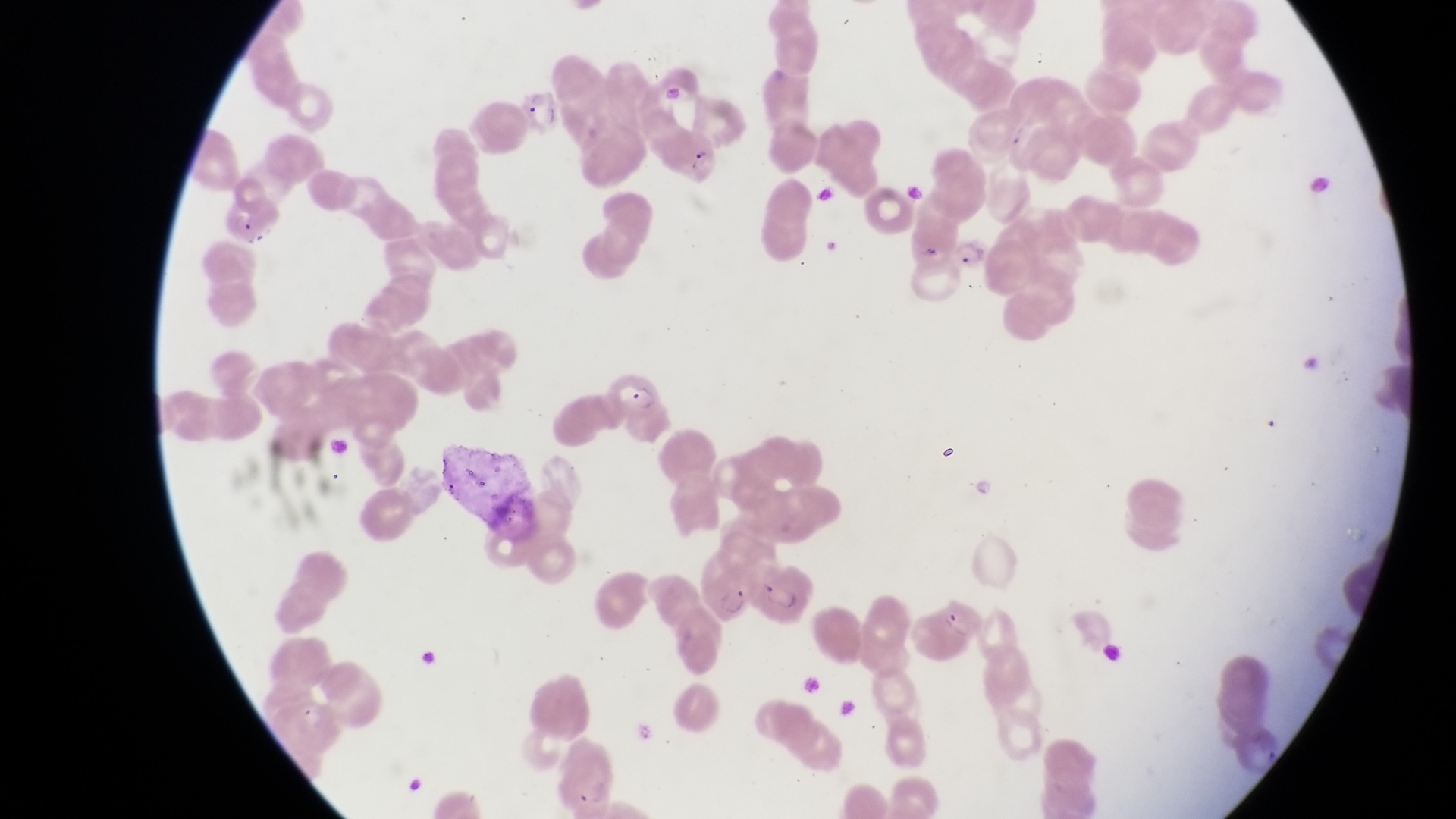

{
  "capture": "smartphone photograph through the eyepiece of an Olympus CX-23 microscope",
  "artifact_platelet_like_body_stain_precipitate_or_debris_locations": "approximate bounding boxes as [left, top, right, bottom] in pixels: [689, 142, 713, 171], [901, 178, 925, 210], [940, 444, 960, 464]",
  "image_size": "1456×819 pixels",
  "trophozoite_locations": "approximate bounding boxes as [left, top, right, bottom] in pixels: [952, 237, 984, 270], [968, 475, 998, 504]",
  "country": "Uganda",
  "parasitised_red_blood_cell_locations": "approximate bounding boxes as [left, top, right, bottom] in pixels: [215, 195, 282, 247], [605, 372, 658, 422], [697, 551, 755, 623], [752, 561, 815, 621]",
  "field_of_view": "single",
  "preparation": "thin blood smear",
  "magnification": "1000x"
}